Assess the morphology of the red blood cells.
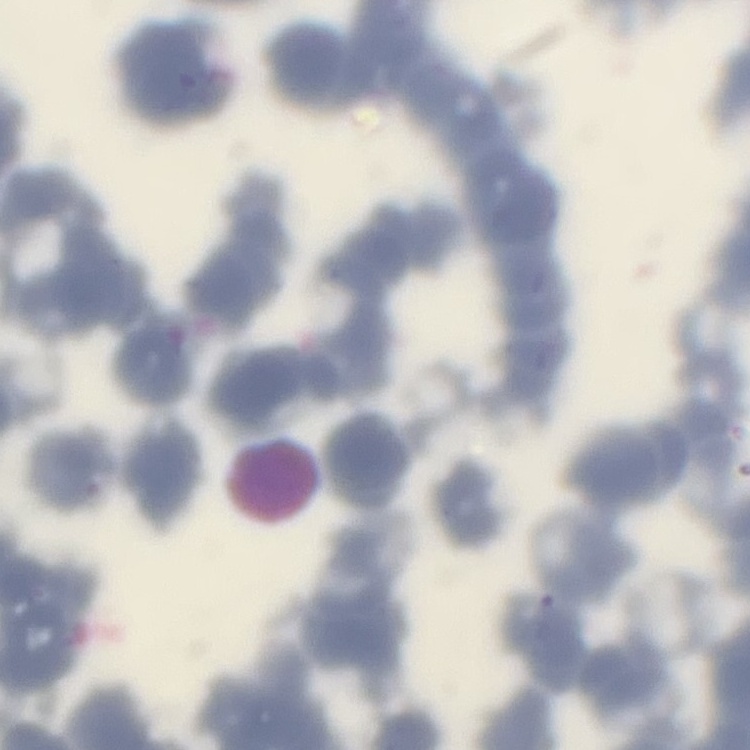
Rouleaux formation.

Thin blood smear. One tile cut from a larger photomicrograph. Field's or Giemsa stain.